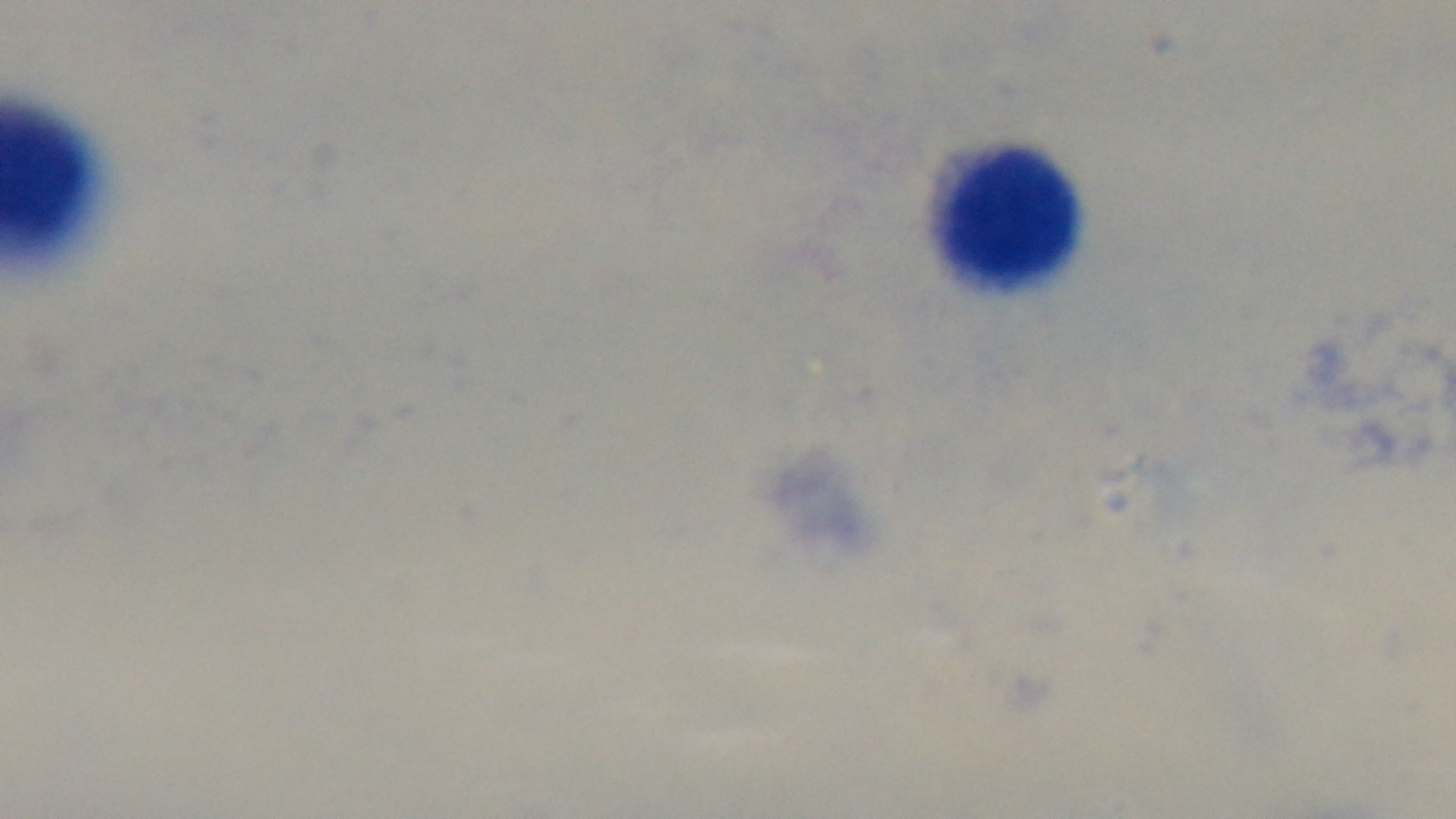
Preparation: thick blood film. Oil-immersion objective, 100x. Captured with a mounted 4K digital camera. Photomicrograph. Giemsa stain. One field from the slide. Malaria status: uninfected.